Assess this cell for malaria.
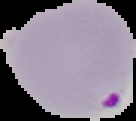
Parasitized.

Summary:
  - Preparation: thin blood smear
  - Image type: cell region segmented out of the field of view; surrounding area masked to black
  - Image size: 136×121 pixels